State the preparation type.
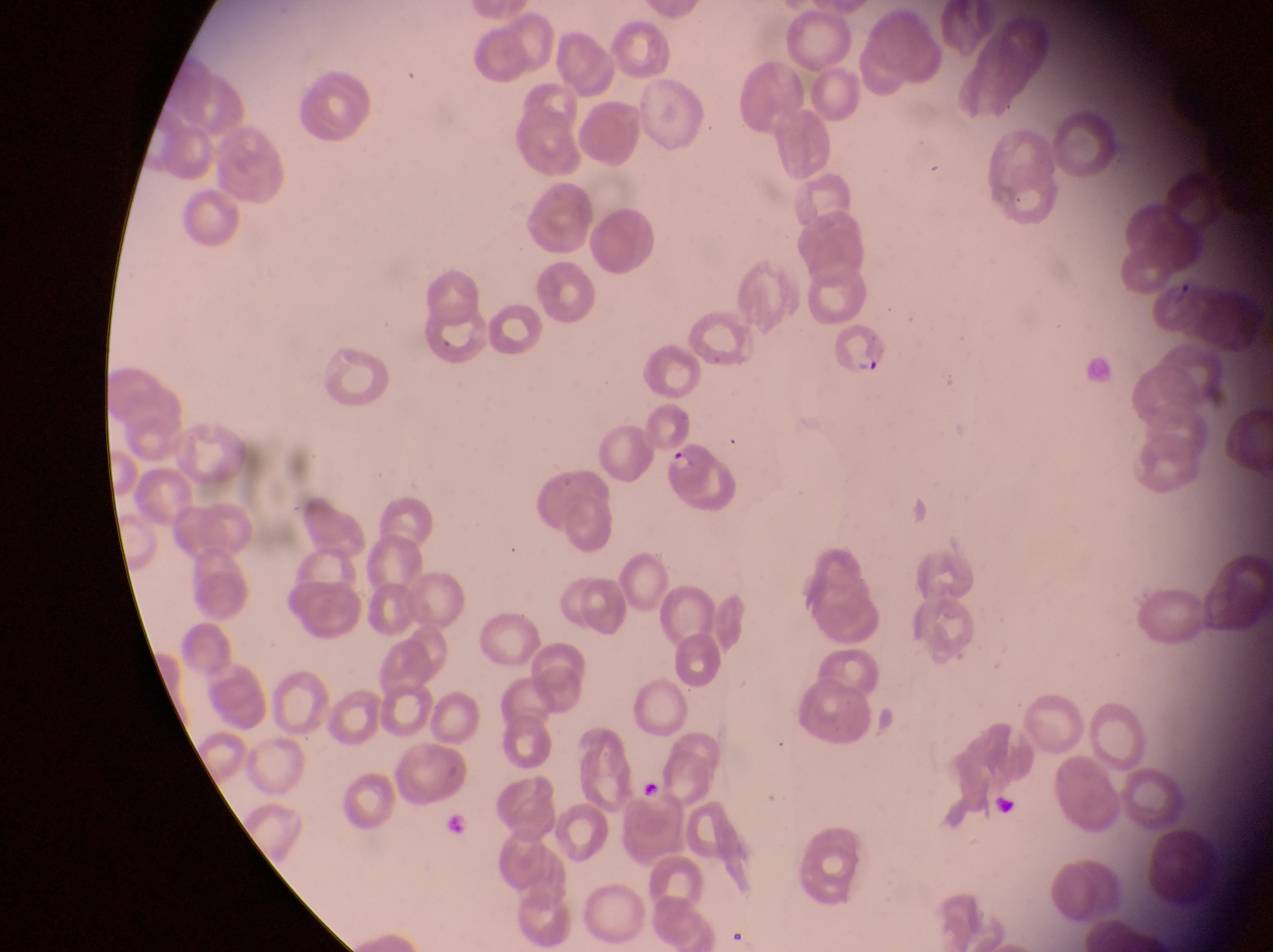

Thin blood smear.

Approximate bounding boxes as [left, top, right, bottom] in pixels.
Summary:
  - Parasitised red blood cell locations: [1157, 276, 1205, 342], [834, 324, 896, 384], [666, 444, 741, 516]
  - Magnification: 1000x
  - Image size: 1273×952 pixels
  - Capture: smartphone photograph through the eyepiece of an Olympus CX-23 microscope
  - Field of view: single
  - Country: Uganda